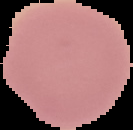 From a thin blood film. Result: no Plasmodium parasites detected. The area outside the segmented cell region is set to black. Image is 133×130 pixels.